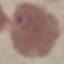 Malaria status: parasitized. Thin blood smear. Giemsa stain. Cell patch, automatically extracted from a larger field of view and resized to 64 × 64 pixels. Acquired by smartphone through the microscope eyepiece.